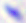
Summary:
  - Magnification: 400x
  - Identification: Toxoplasma gondii
  - Modality: micrograph